Name the cell type shown.
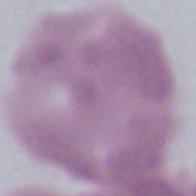
This is an erythrocyte.

modality: micrograph
magnification: 1000x